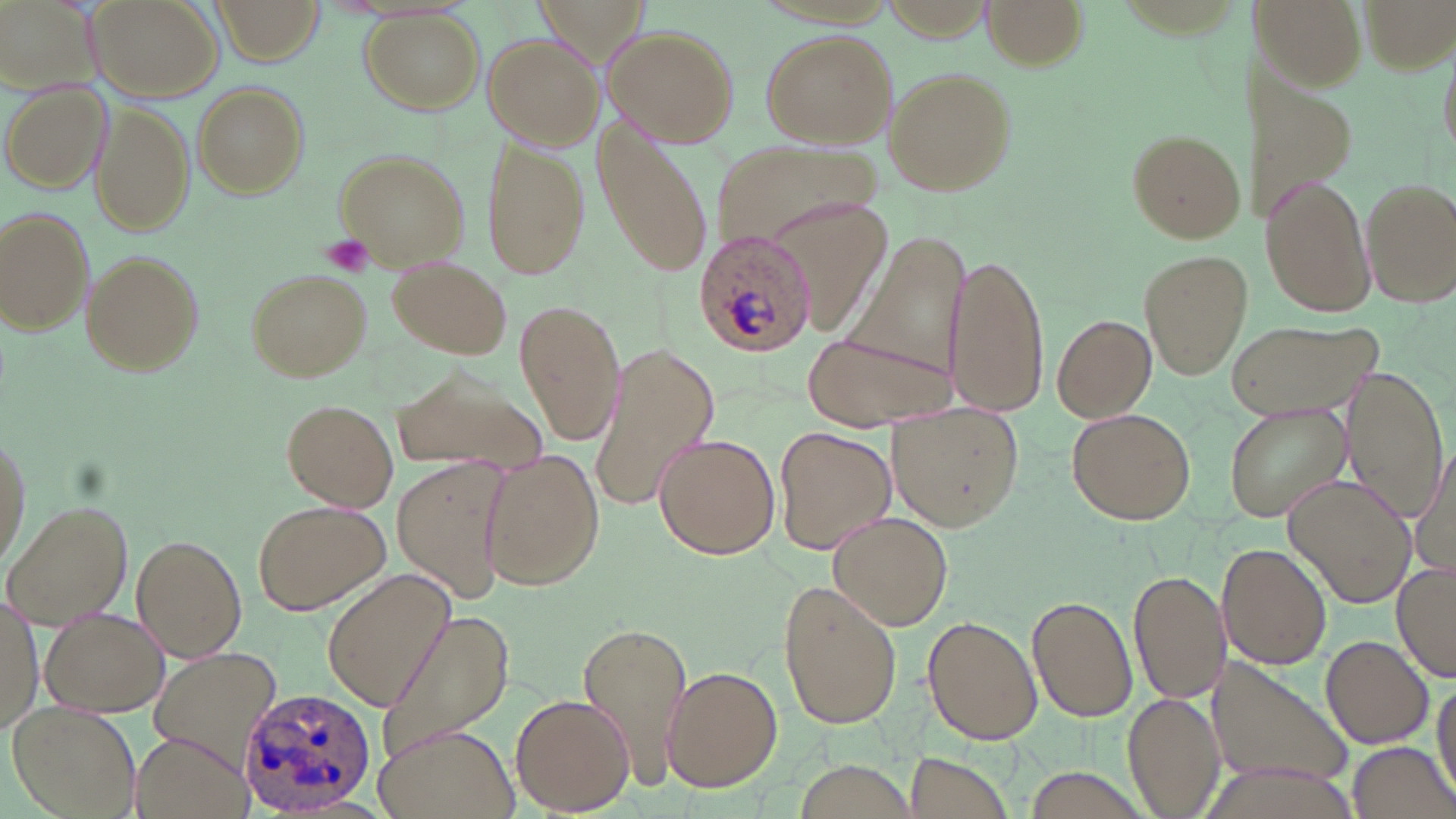
Approximate bounding boxes as (x1, y1, x2, y2) in pixels. Platelet locations: (321, 234, 374, 278). Plasmodium ovale-infected red blood cell locations: (692, 228, 818, 357), (232, 685, 372, 815). Uninfected red blood cell locations: (0, 0, 98, 103), (85, 0, 225, 102), (984, 0, 1088, 71), (1245, 1, 1372, 98), (211, 2, 321, 63), (361, 11, 484, 113), (602, 25, 740, 149), (761, 29, 895, 149), (482, 34, 603, 148), (1235, 43, 1359, 232), (1438, 43, 1455, 167), (882, 64, 1019, 197), (3, 82, 110, 193), (192, 83, 307, 198), (90, 103, 194, 237), (593, 118, 713, 277), (1127, 128, 1247, 243), (480, 135, 591, 281), (711, 139, 886, 256), (333, 146, 469, 268), (1261, 175, 1377, 316), (1362, 178, 1455, 305), (790, 196, 894, 343), (1, 208, 95, 337), (839, 231, 975, 383), (82, 250, 205, 374), (1139, 250, 1250, 378), (947, 254, 1048, 416), (387, 257, 511, 358), (245, 267, 372, 382), (517, 299, 623, 446), (1051, 314, 1156, 422), (1225, 317, 1383, 422), (804, 331, 954, 431), (588, 344, 719, 518), (391, 356, 549, 484), (1343, 365, 1450, 524), (280, 398, 398, 510), (1222, 401, 1350, 522), (889, 407, 1026, 532), (1067, 407, 1196, 526), (1, 426, 31, 570), (773, 426, 895, 555), (654, 432, 780, 559), (1408, 447, 1455, 579), (479, 451, 604, 590), (395, 461, 509, 600), (1283, 473, 1417, 609), (250, 498, 390, 616), (4, 500, 133, 628), (832, 512, 953, 627), (131, 533, 247, 661), (1217, 541, 1333, 670), (1394, 561, 1455, 683), (1130, 567, 1229, 705), (322, 570, 458, 714), (778, 580, 902, 732), (0, 591, 41, 736), (1026, 595, 1137, 722), (41, 606, 168, 716), (377, 607, 517, 761), (574, 615, 693, 781), (923, 615, 1043, 745), (1320, 634, 1433, 749), (149, 649, 280, 769), (1208, 656, 1355, 792), (659, 665, 784, 793), (1432, 676, 1455, 801), (1122, 691, 1224, 819), (511, 692, 636, 815), (9, 701, 141, 819), (374, 724, 520, 819), (133, 732, 251, 819), (1345, 740, 1456, 819), (901, 750, 1019, 819), (792, 760, 916, 819). Slide-level diagnosis: Plasmodium ovale. Thin blood smear. May-Grünwald-Giemsa-stained preparation. Image is 1456×819 pixels. 1000x magnification. Optical microscopy. Single field of view.